State which parasite is depicted.
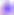
This is Toxoplasma gondii.

magnification = 400x
modality = micrograph